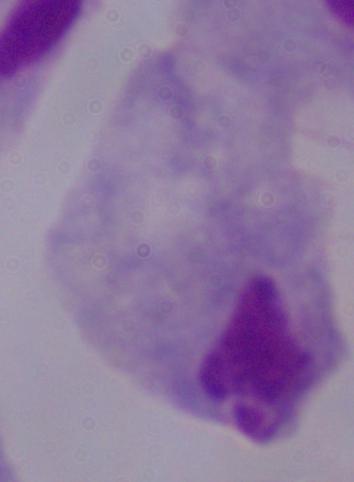
modality: photomicrograph
magnification: 1000x
identification: trichomonad